Outline platelets.
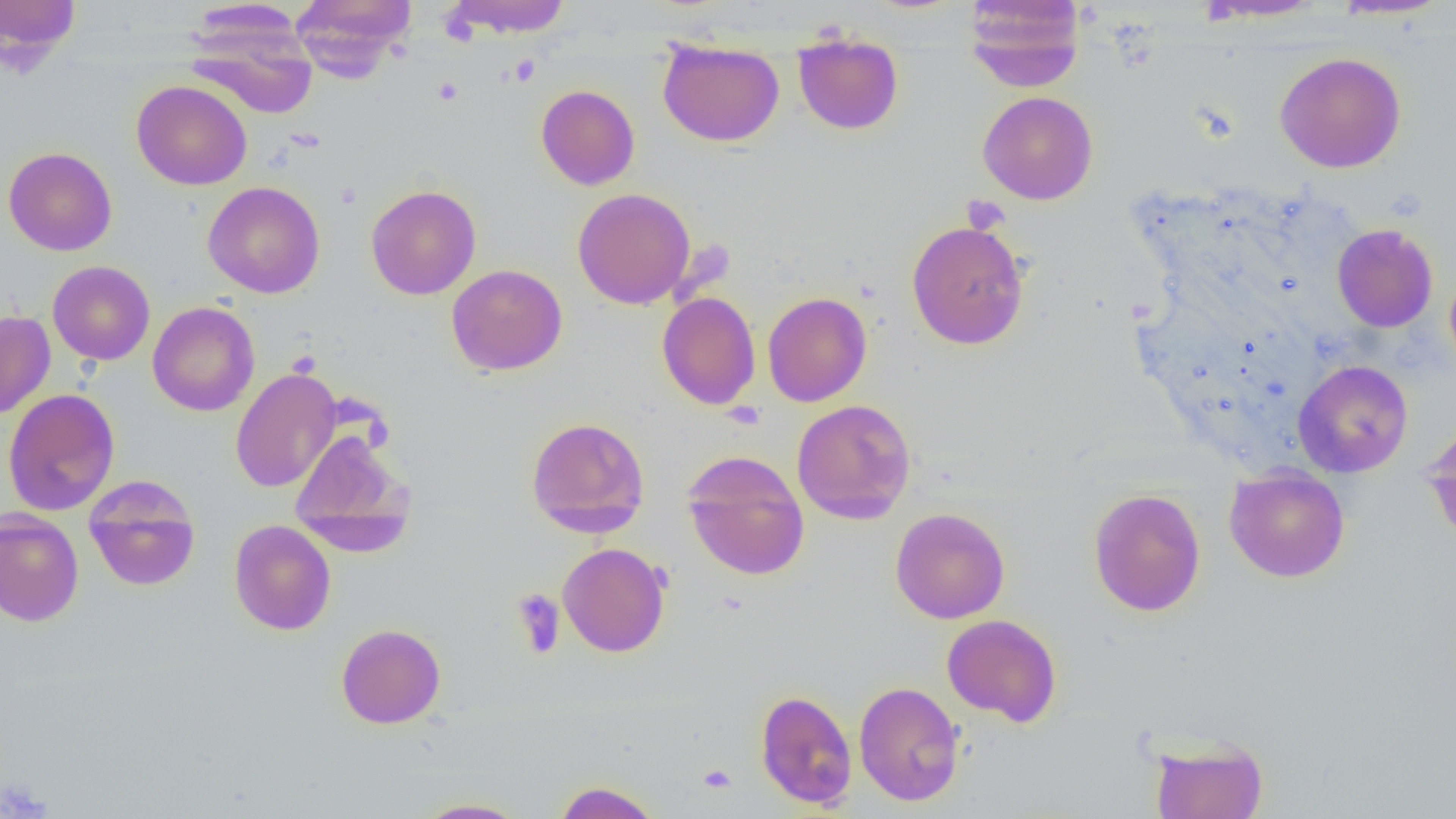
Approximate bounding boxes as (x1, y1, x2, y2) in pixels.
Platelets: (509, 55, 540, 85), (961, 195, 1010, 235), (511, 588, 565, 659), (697, 763, 737, 794), (0, 776, 52, 818).

Summary:
  - Uninfected red blood cell locations: (0, 0, 82, 64), (291, 0, 416, 78), (445, 0, 573, 37), (963, 0, 1086, 91), (1198, 0, 1327, 21), (1329, 0, 1453, 20), (186, 13, 318, 119), (793, 33, 903, 135), (658, 41, 784, 146), (1274, 52, 1406, 173), (131, 80, 252, 190), (535, 84, 640, 190), (978, 91, 1098, 205), (3, 147, 117, 255), (202, 181, 325, 298), (365, 184, 481, 300), (572, 188, 696, 309), (906, 220, 1030, 349), (1332, 224, 1438, 332), (47, 260, 155, 365), (1444, 263, 1456, 379), (446, 264, 568, 376), (657, 291, 760, 410), (762, 291, 872, 407), (147, 301, 259, 416), (0, 311, 55, 418), (1293, 359, 1413, 478), (230, 367, 342, 493), (3, 389, 121, 516), (791, 399, 916, 524), (526, 416, 650, 537), (1422, 420, 1456, 546), (288, 428, 413, 550), (682, 451, 810, 581), (1224, 466, 1350, 582), (83, 475, 200, 591), (1088, 488, 1206, 616), (890, 507, 1010, 623), (0, 509, 84, 626), (229, 519, 337, 635), (557, 542, 670, 657), (941, 614, 1062, 726), (336, 623, 446, 728), (853, 681, 964, 806), (755, 689, 857, 809), (1149, 737, 1269, 819), (552, 780, 663, 819), (413, 797, 532, 818)
  - Slide-level diagnosis: negative for blood parasites
  - Magnification: 1000x
  - Modality: light microscopy
  - Field of view: one of a larger specimen
  - Preparation: thin blood film
  - Image size: 1456×819 pixels